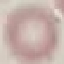
Malaria status: uninfected. Cell patch, automatically extracted from a larger field of view and resized to 64 × 64 pixels. Giemsa stain. Acquired by smartphone through the microscope eyepiece. Thin smear of blood.